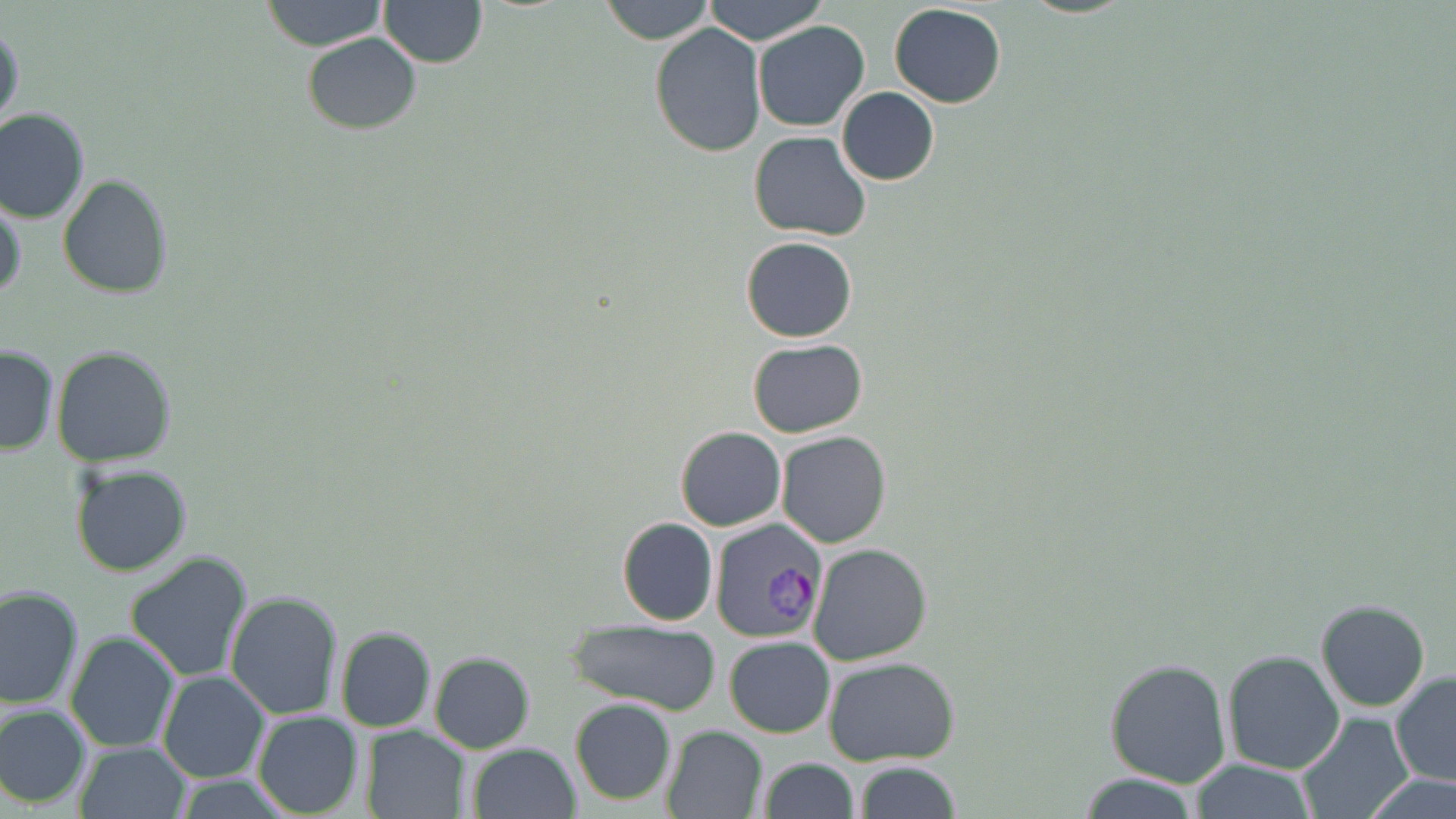

slide-level diagnosis = Plasmodium vivax
modality = optical microscopy
image size = 1456×819 pixels
preparation = thin blood smear
uninfected red blood cell locations = approximate bounding boxes as [x1, y1, x2, y2] in pixels: [259, 0, 389, 51], [378, 0, 487, 68], [600, 0, 715, 44], [702, 0, 827, 44], [888, 4, 1007, 108], [752, 20, 870, 133], [0, 21, 22, 132], [649, 22, 766, 157], [301, 33, 422, 134], [836, 87, 940, 186], [0, 108, 91, 222], [749, 131, 873, 240], [57, 173, 172, 299], [0, 191, 28, 305], [740, 237, 856, 342], [747, 339, 868, 437], [0, 345, 58, 455], [51, 345, 178, 466], [675, 426, 787, 531], [776, 430, 890, 548], [69, 461, 194, 576], [617, 517, 718, 626], [806, 544, 931, 667], [125, 552, 252, 681], [0, 585, 85, 712], [225, 589, 345, 720], [1314, 598, 1430, 713], [565, 620, 723, 715], [335, 626, 437, 732], [65, 631, 180, 754], [725, 635, 835, 737], [1221, 649, 1344, 774], [428, 651, 536, 753], [824, 657, 960, 767], [1104, 659, 1233, 787], [158, 670, 270, 783], [1389, 671, 1456, 788], [570, 698, 676, 805], [0, 704, 91, 808], [252, 711, 363, 818], [1296, 712, 1414, 819], [360, 726, 470, 817], [661, 726, 767, 818], [75, 740, 192, 819], [464, 742, 581, 819], [759, 758, 860, 819], [1188, 759, 1317, 818], [854, 761, 962, 819], [1079, 772, 1200, 819], [1366, 773, 1456, 819]
stain = May-Grünwald-Giemsa
magnification = 1000x
Plasmodium vivax-infected red blood cell locations = approximate bounding boxes as [x1, y1, x2, y2] in pixels: [708, 520, 827, 643]
field of view = single